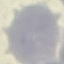
Summary:
  - Malaria status: uninfected
  - Stain: Giemsa
  - Capture: smartphone camera at the microscope eyepiece
  - Preparation: thin blood film
  - Image type: automatically extracted cell patch, resized to 64 × 64 pixels